Identify the parasite.
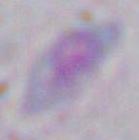
This is Toxoplasma gondii.

modality: photomicrograph
magnification: 1000x